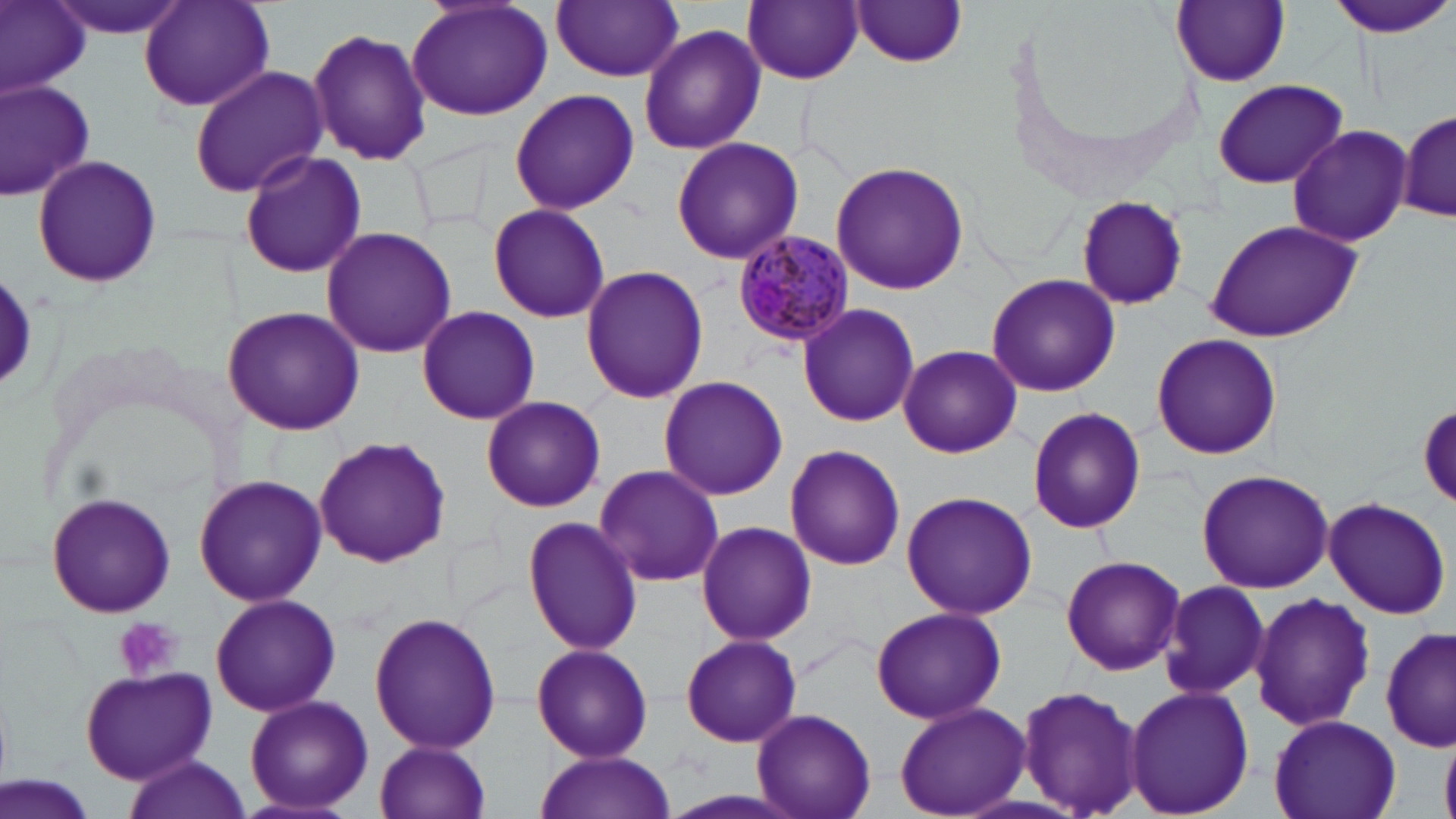 Approximate bounding boxes as named x1/y1/x2/y2 corners in pixels. Uninfected red blood cell locations: (x1=0, y1=0, x2=90, y2=96), (x1=47, y1=0, x2=191, y2=40), (x1=138, y1=0, x2=277, y2=113), (x1=405, y1=0, x2=553, y2=123), (x1=744, y1=0, x2=862, y2=85), (x1=1326, y1=0, x2=1455, y2=37), (x1=551, y1=1, x2=685, y2=81), (x1=1171, y1=1, x2=1289, y2=87), (x1=851, y1=2, x2=967, y2=69), (x1=638, y1=23, x2=766, y2=157), (x1=306, y1=26, x2=434, y2=168), (x1=190, y1=64, x2=330, y2=195), (x1=0, y1=77, x2=97, y2=201), (x1=1210, y1=77, x2=1349, y2=189), (x1=509, y1=89, x2=639, y2=215), (x1=1395, y1=109, x2=1454, y2=226), (x1=1286, y1=123, x2=1414, y2=247), (x1=670, y1=136, x2=804, y2=266), (x1=413, y1=138, x2=495, y2=231), (x1=237, y1=150, x2=367, y2=280), (x1=30, y1=156, x2=163, y2=288), (x1=831, y1=162, x2=968, y2=295), (x1=1075, y1=195, x2=1189, y2=313), (x1=486, y1=203, x2=611, y2=322), (x1=1204, y1=218, x2=1363, y2=343), (x1=320, y1=226, x2=456, y2=359), (x1=580, y1=264, x2=708, y2=404), (x1=0, y1=269, x2=41, y2=399), (x1=986, y1=273, x2=1120, y2=398), (x1=797, y1=303, x2=919, y2=428), (x1=415, y1=305, x2=541, y2=426), (x1=221, y1=306, x2=367, y2=435), (x1=1150, y1=333, x2=1281, y2=461), (x1=899, y1=345, x2=1020, y2=457), (x1=656, y1=375, x2=788, y2=501), (x1=481, y1=395, x2=606, y2=513), (x1=1415, y1=402, x2=1456, y2=506), (x1=1026, y1=406, x2=1148, y2=536), (x1=313, y1=436, x2=451, y2=569), (x1=783, y1=444, x2=907, y2=572), (x1=591, y1=464, x2=726, y2=589), (x1=1195, y1=468, x2=1333, y2=593), (x1=194, y1=475, x2=328, y2=608), (x1=46, y1=491, x2=176, y2=619), (x1=902, y1=491, x2=1037, y2=619), (x1=1321, y1=496, x2=1452, y2=619), (x1=520, y1=516, x2=644, y2=655), (x1=694, y1=520, x2=817, y2=648), (x1=1061, y1=554, x2=1182, y2=675), (x1=1160, y1=581, x2=1271, y2=702), (x1=209, y1=593, x2=341, y2=718), (x1=1249, y1=593, x2=1377, y2=730), (x1=870, y1=605, x2=1007, y2=725), (x1=368, y1=610, x2=502, y2=755), (x1=1381, y1=625, x2=1454, y2=754), (x1=680, y1=634, x2=802, y2=748), (x1=530, y1=641, x2=654, y2=762), (x1=79, y1=667, x2=218, y2=785), (x1=1016, y1=682, x2=1144, y2=819), (x1=1125, y1=685, x2=1255, y2=817), (x1=244, y1=695, x2=374, y2=814), (x1=894, y1=702, x2=1028, y2=818), (x1=752, y1=707, x2=877, y2=819), (x1=1269, y1=714, x2=1401, y2=819), (x1=1439, y1=731, x2=1456, y2=819), (x1=373, y1=739, x2=493, y2=819), (x1=535, y1=752, x2=672, y2=819), (x1=122, y1=757, x2=252, y2=819), (x1=1, y1=777, x2=100, y2=819). Platelet locations: (x1=113, y1=617, x2=184, y2=682). Plasmodium malariae-infected red blood cell locations: (x1=735, y1=230, x2=853, y2=350). Slide-level diagnosis: Plasmodium malariae. Captured at 1000x magnification. Image is 1456×819 pixels. May-Grünwald-Giemsa-stained preparation. Light microscopy. One field of a larger specimen. Thin blood smear.